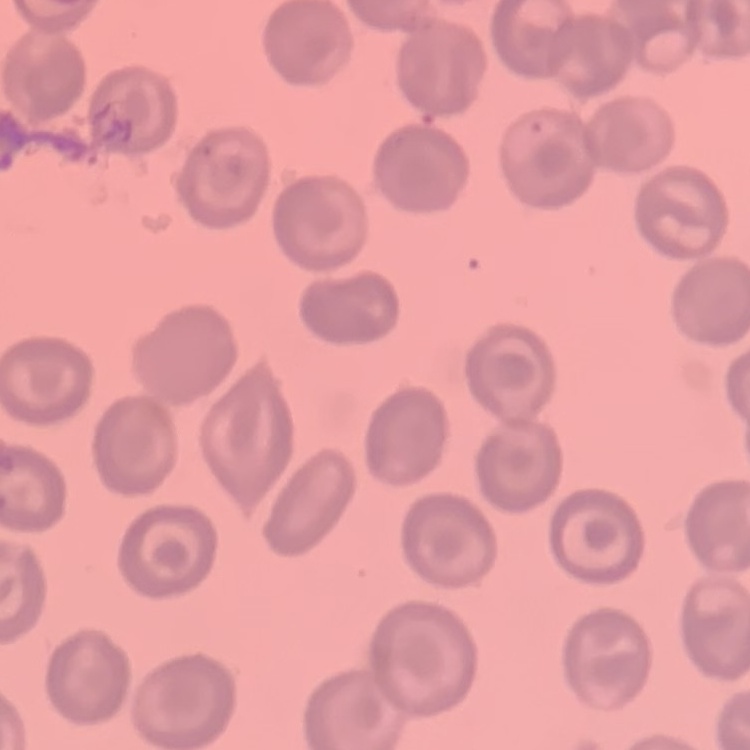
The red blood cells exhibit no rouleaux formation. Stained with either Field's or Giemsa. One tile cut from a larger photomicrograph. Thin blood smear.